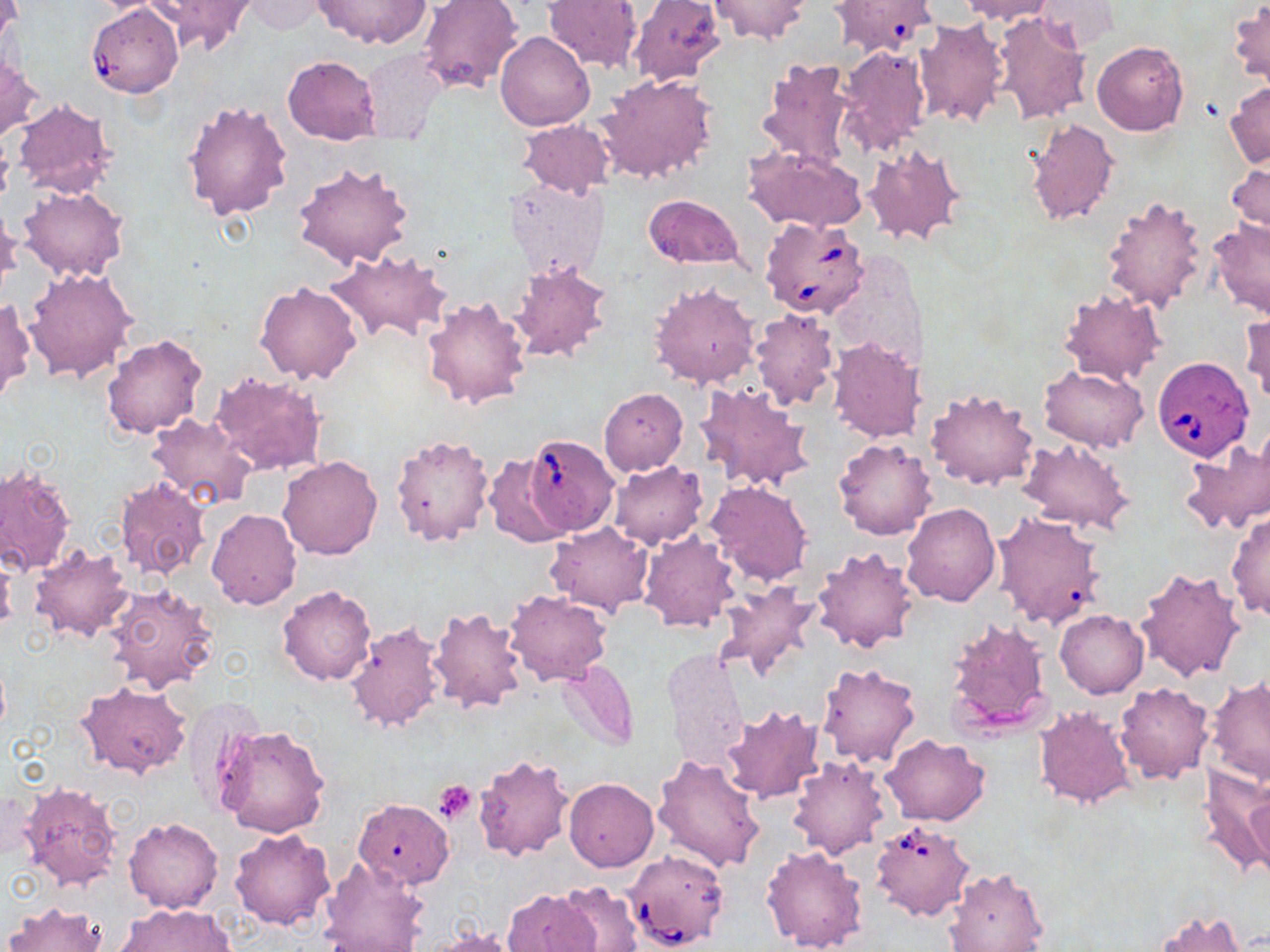

Summary:
  - Coordinate format: approximate bounding boxes as (x1, y1, x2, y2) in pixels
  - Uninfected red blood cell locations: (148, 0, 256, 56), (313, 0, 431, 49), (543, 0, 644, 73), (627, 0, 727, 86), (710, 0, 811, 43), (830, 0, 938, 58), (959, 0, 1057, 24), (1, 1, 21, 55), (240, 1, 329, 35), (418, 1, 523, 93), (1035, 1, 1118, 53), (1229, 3, 1269, 86), (992, 11, 1092, 126), (913, 16, 1009, 129), (496, 32, 593, 131), (1092, 42, 1188, 136), (836, 44, 932, 155), (357, 49, 449, 146), (282, 55, 381, 143), (757, 57, 860, 169), (0, 58, 42, 141), (597, 72, 718, 185), (1225, 82, 1270, 169), (182, 99, 293, 220), (11, 100, 115, 198), (1024, 117, 1119, 224), (517, 120, 615, 198), (862, 142, 966, 247), (743, 146, 867, 232), (292, 159, 416, 270), (1227, 160, 1270, 241), (505, 178, 611, 282), (17, 184, 129, 282), (643, 193, 744, 270), (1101, 195, 1210, 314), (0, 206, 22, 295), (936, 212, 1006, 277), (1208, 219, 1270, 321), (323, 248, 452, 347), (510, 261, 614, 364), (24, 268, 139, 385), (255, 281, 362, 384), (649, 282, 761, 390), (1059, 289, 1163, 386), (420, 296, 531, 412), (0, 299, 35, 406), (751, 308, 840, 411), (1243, 310, 1269, 409), (101, 334, 207, 438), (827, 337, 927, 444), (1039, 365, 1148, 452), (209, 370, 328, 478), (695, 381, 815, 493), (599, 387, 688, 476), (924, 387, 1038, 491), (146, 413, 255, 511), (390, 433, 494, 546), (1179, 436, 1270, 536), (833, 437, 937, 540), (1019, 439, 1136, 536), (483, 453, 576, 547), (276, 455, 383, 560), (608, 461, 708, 548), (1, 464, 75, 575), (115, 477, 213, 582), (706, 480, 812, 587), (902, 503, 1000, 607), (207, 508, 302, 610), (993, 511, 1105, 629), (1227, 511, 1270, 622), (544, 522, 653, 614), (640, 531, 741, 633), (28, 545, 136, 643), (811, 547, 920, 653), (0, 556, 17, 634), (1135, 566, 1245, 684), (717, 581, 824, 682), (103, 583, 220, 693), (277, 585, 377, 686), (503, 590, 611, 686), (428, 604, 529, 714), (1055, 610, 1148, 698), (945, 618, 1052, 737), (343, 620, 445, 734), (663, 647, 749, 768), (557, 660, 641, 750), (815, 661, 921, 768), (1206, 677, 1270, 787), (79, 681, 192, 777), (1115, 682, 1214, 784), (182, 695, 267, 812), (719, 704, 825, 804), (1034, 705, 1135, 808), (216, 726, 331, 839), (881, 734, 989, 827), (474, 752, 574, 862), (652, 754, 764, 873), (787, 754, 891, 860), (1197, 765, 1270, 877), (564, 778, 658, 871), (21, 783, 120, 891), (1245, 793, 1270, 879), (354, 798, 454, 889), (123, 817, 224, 913), (228, 828, 336, 931), (762, 845, 871, 952), (318, 857, 430, 952), (944, 866, 1048, 952), (554, 885, 640, 952), (502, 888, 601, 952), (3, 901, 106, 952), (115, 903, 235, 952), (1156, 911, 1249, 952), (421, 929, 521, 952)
  - Babesia divergens-infected red blood cell locations: (87, 4, 184, 97), (760, 216, 870, 318), (1152, 356, 1253, 461), (520, 433, 620, 536), (869, 819, 975, 921), (623, 848, 731, 952)
  - Platelet locations: (434, 781, 478, 825)
  - Slide-level diagnosis: Babesia divergens
  - Field of view: single
  - Modality: light microscopy
  - Image size: 1270×952 pixels
  - Preparation: thin blood film
  - Stain: May-Grünwald-Giemsa
  - Magnification: 1000x